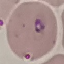
{
  "malaria_status": "parasitized",
  "preparation": "thin blood film",
  "stain": "Giemsa",
  "image_type": "automatically extracted cell patch, resized to 64 × 64 pixels",
  "capture": "smartphone camera at the microscope eyepiece"
}